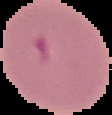

image_type: segmented cell region with the area outside set to black
image_size: 112×115 pixels
malaria_status: parasitized
preparation: thin blood film